Classify this cell by malaria status.
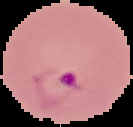
Parasitized.

preparation = thin blood smear
image type = cell region segmented out of the field of view; surrounding area masked to black
image size = 133×127 pixels